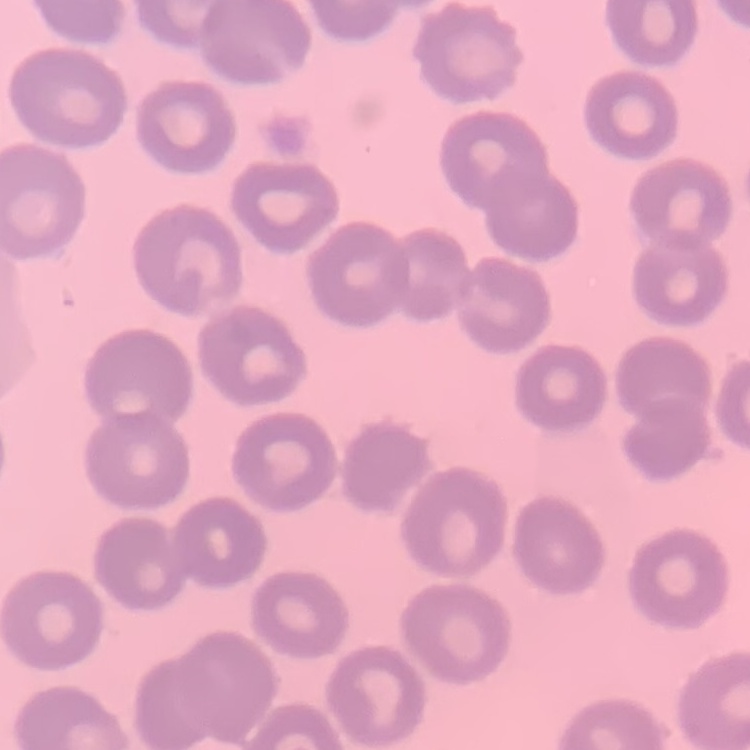

Summary:
  - Erythrocyte morphology: no rouleaux formation
  - Preparation: thin blood film
  - Image type: one tile cut from a larger photomicrograph
  - Stain: Field's or Giemsa